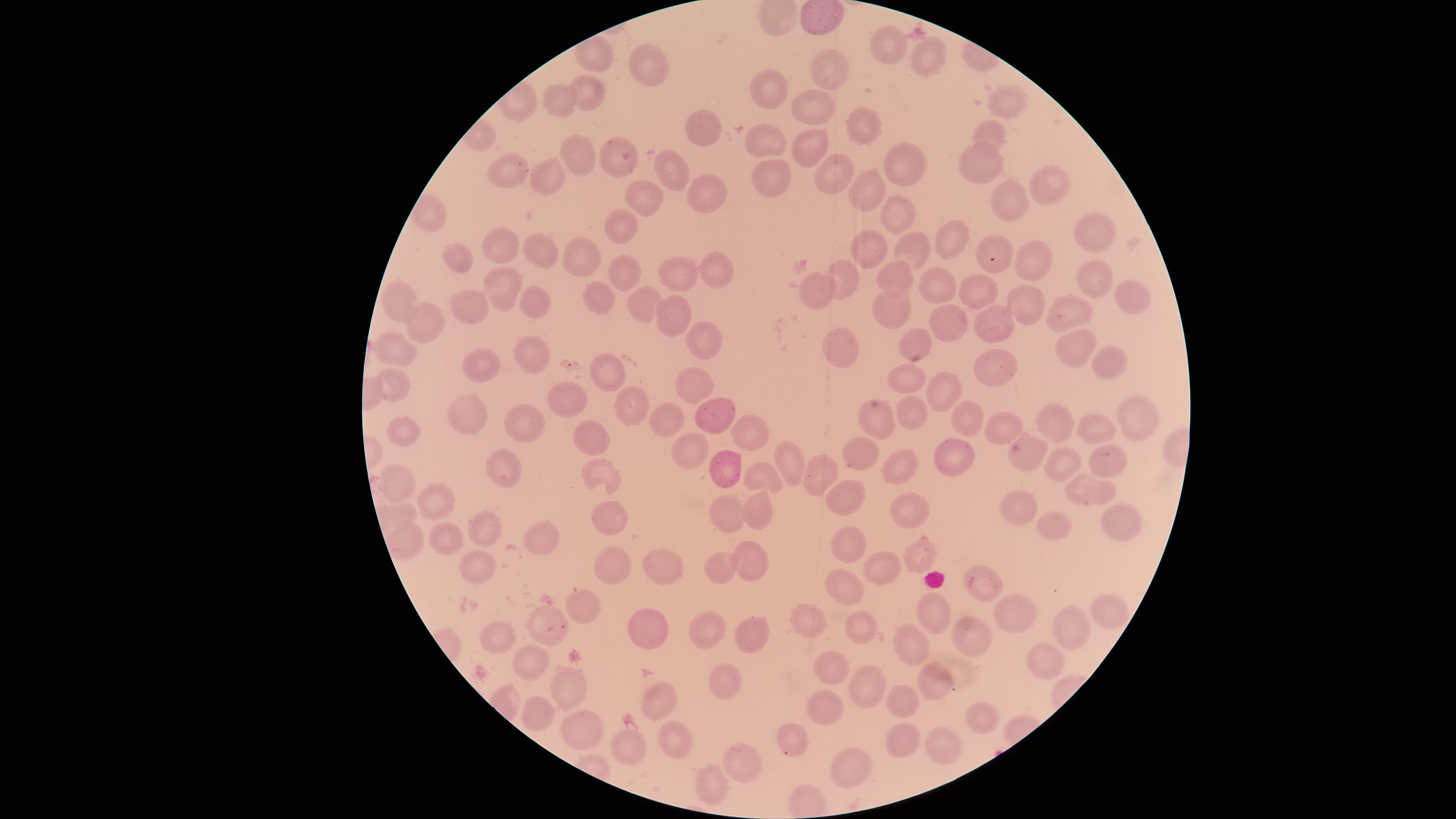
Approximate marker points as (x, y) in pixels.
Summary:
  - Uninfected RBCs: (885, 47), (925, 56), (827, 70), (649, 73), (768, 93), (588, 95), (1006, 104), (559, 105), (813, 110), (864, 128), (703, 134), (989, 136), (765, 141), (808, 147), (582, 155), (983, 156), (617, 160), (906, 164), (837, 169), (669, 174), (510, 175), (548, 176), (771, 177), (1047, 182), (871, 186), (700, 195), (1014, 199), (642, 203), (897, 209), (621, 229), (1095, 236), (954, 239), (502, 244), (539, 248), (994, 248), (913, 249), (872, 251), (455, 259), (586, 262), (1033, 262), (708, 266), (624, 273), (675, 274), (894, 274), (1095, 274), (843, 279), (494, 286), (942, 288), (975, 288), (595, 295), (816, 295), (1127, 296), (393, 299), (533, 300), (645, 304), (1026, 306), (468, 309), (892, 309), (1073, 313), (992, 316), (668, 317), (951, 320), (427, 321), (704, 338), (845, 341), (916, 343), (395, 346), (1077, 346), (1101, 357), (533, 358), (472, 365), (982, 367), (609, 373), (389, 378), (907, 378), (694, 379), (949, 391), (566, 393), (634, 400), (911, 411), (481, 415), (717, 415), (966, 415), (1135, 416), (525, 417), (876, 418), (664, 419), (1060, 422), (1003, 423), (1102, 425), (752, 430), (412, 433), (594, 436), (685, 450), (858, 456), (1029, 456), (1109, 458), (951, 459), (509, 460), (728, 461), (1066, 463), (786, 464), (900, 471), (817, 472), (755, 477), (603, 479), (398, 481), (1085, 487), (848, 493), (436, 500), (1020, 504), (756, 508), (908, 508), (726, 510), (607, 518), (1054, 519), (1124, 521), (484, 532), (850, 539), (538, 540), (407, 541), (917, 551), (747, 557), (610, 564), (484, 565), (880, 567), (663, 568), (724, 572), (847, 584), (986, 585), (583, 605), (935, 609), (1116, 609), (1023, 615), (802, 619), (862, 622), (554, 624), (755, 625), (1070, 630), (648, 632), (502, 634), (707, 635), (967, 637), (914, 644), (533, 664), (839, 667), (1043, 668), (727, 682), (931, 683), (568, 686), (869, 690), (658, 694), (905, 702), (825, 711), (540, 713), (980, 713), (578, 725), (633, 735), (900, 737), (678, 743), (789, 744), (939, 747), (741, 764), (850, 765), (707, 786)
  - Field of view: single
  - Stain: Giemsa
  - Preparation: thin blood smear
  - Image size: 1456×819 pixels
  - Visible region: circular
  - Presence: no malaria parasites detected
  - Capture: smartphone photograph through the microscope eyepiece